Identify the parasite.
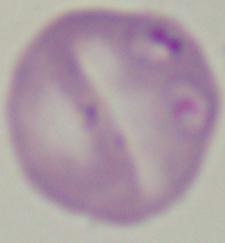
Babesia.

Summary:
  - Magnification: 1000x
  - Modality: photomicrograph